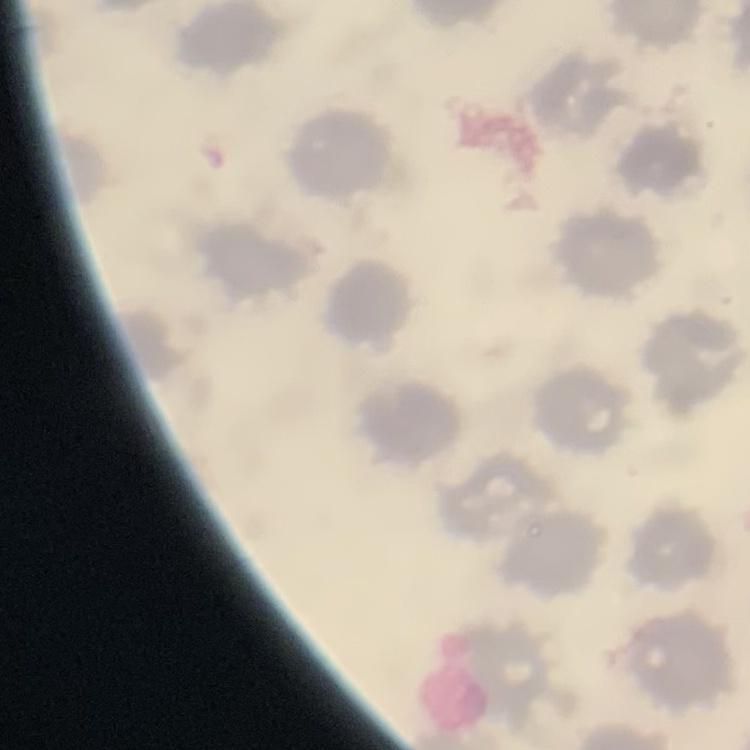

Summary:
  - Red blood cell morphology: no rouleaux formation
  - Preparation: thin peripheral smear
  - Stain: Field's or Giemsa
  - Image type: one tile cut from a larger photomicrograph